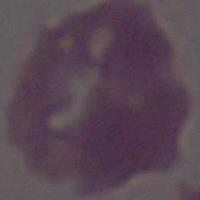

Summary:
  - Identification: red blood cell
  - Modality: photomicrograph
  - Magnification: 1000x